Give the position of every malaria parasite.
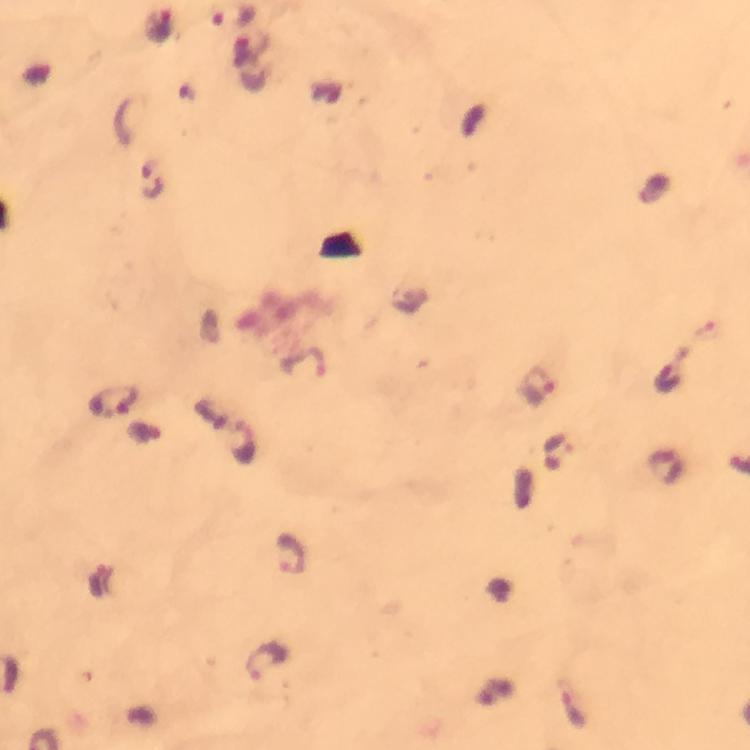
Approximate centers as [x, y] in pixels.
Malaria parasites: [151, 179], [536, 386], [116, 400], [290, 554], [265, 660], [571, 707].

Thick blood film. Cropped region of a single field of view. Immersion oil was used. Image is 750×750 pixels. 100x magnification. From a diagnostic examination for malaria. Giemsa stain. Photographed with a smartphone mounted on the microscope.